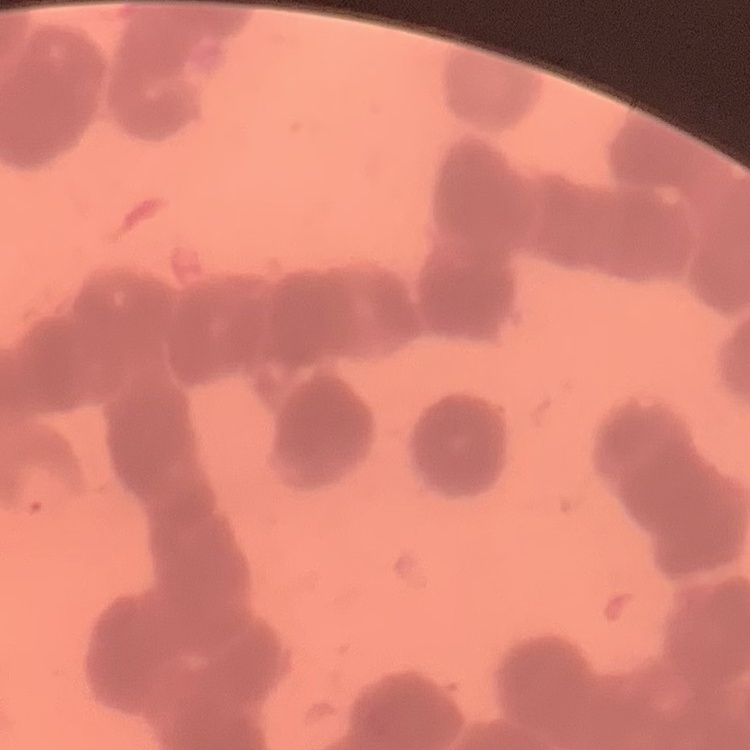

The red blood cells show rouleaux formation. Stained with either Field's or Giemsa. Thin peripheral smear. Square crop of a larger photomicrograph.